Locate every Plasmodium parasite by life-cycle stage, and every leukocyte.
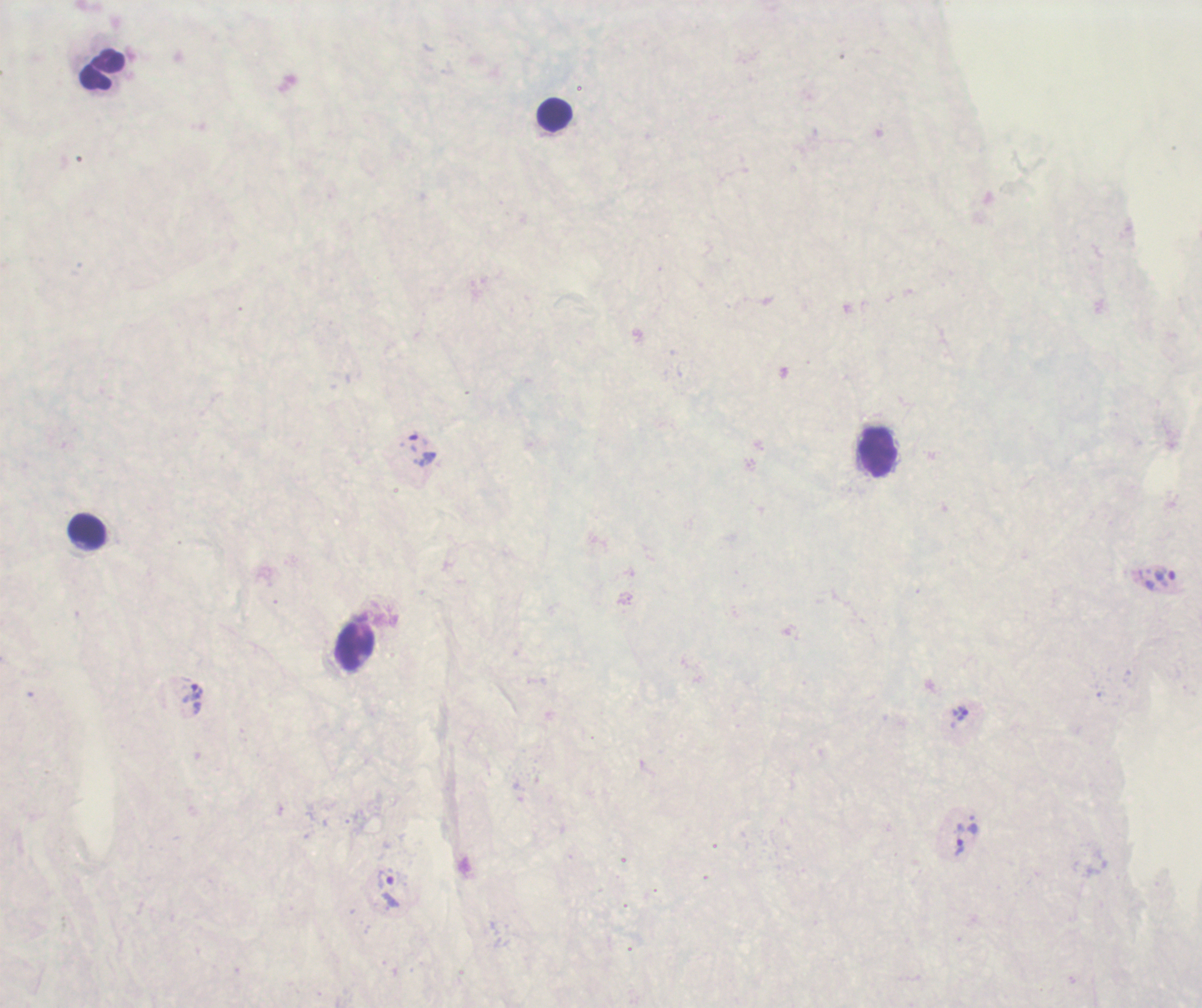
Approximate object centers, in pixels from the top-left corner.
Trophozoites: (x=423, y=449), (x=1164, y=578), (x=192, y=692), (x=960, y=713), (x=959, y=839), (x=385, y=881).
No schizont or gametocyte forms observed.
Leukocytes: (x=102, y=70), (x=555, y=115), (x=878, y=453), (x=88, y=531), (x=355, y=648).

Coloration quality: bad. Previously used in an actual diagnosis. Background quality: unsatisfactory. Thick blood film. Single field of view. Romanowsky-stained preparation. Captured at 100x magnification. Image is 1202×1008 pixels.